Describe the morphology of the red blood cells.
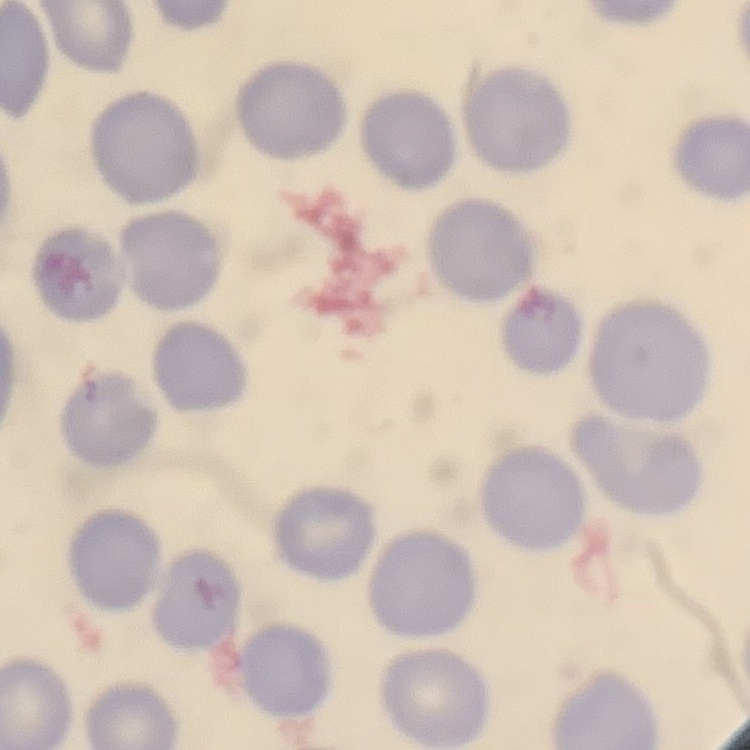
They show no rouleaux formation.

preparation = thin blood smear
image type = square crop of a larger photomicrograph
stain = Field's or Giemsa